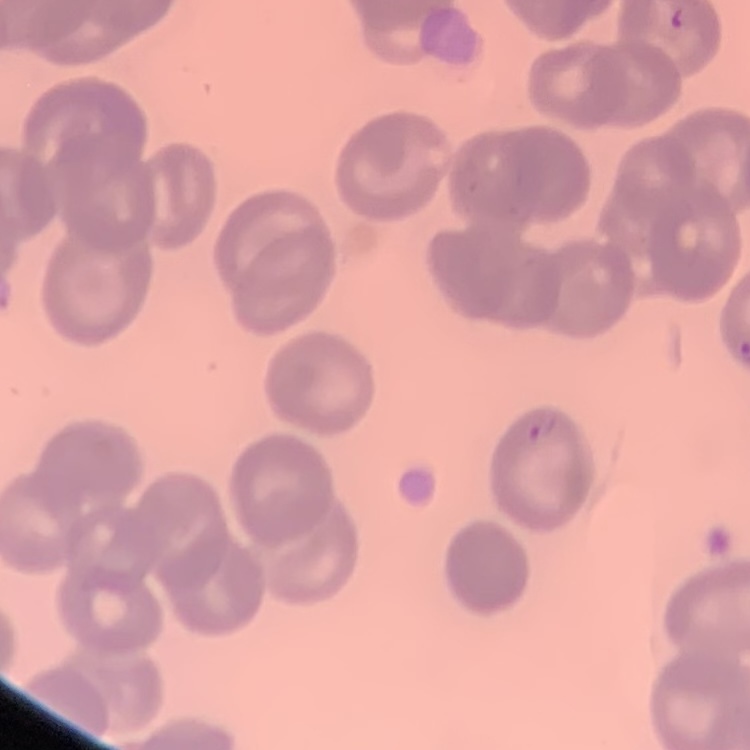
The red blood cells show no rouleaux formation. Thin peripheral smear. Field's or Giemsa stain. Square crop of a larger photomicrograph.